Give the position of every Plasmodium parasite visible.
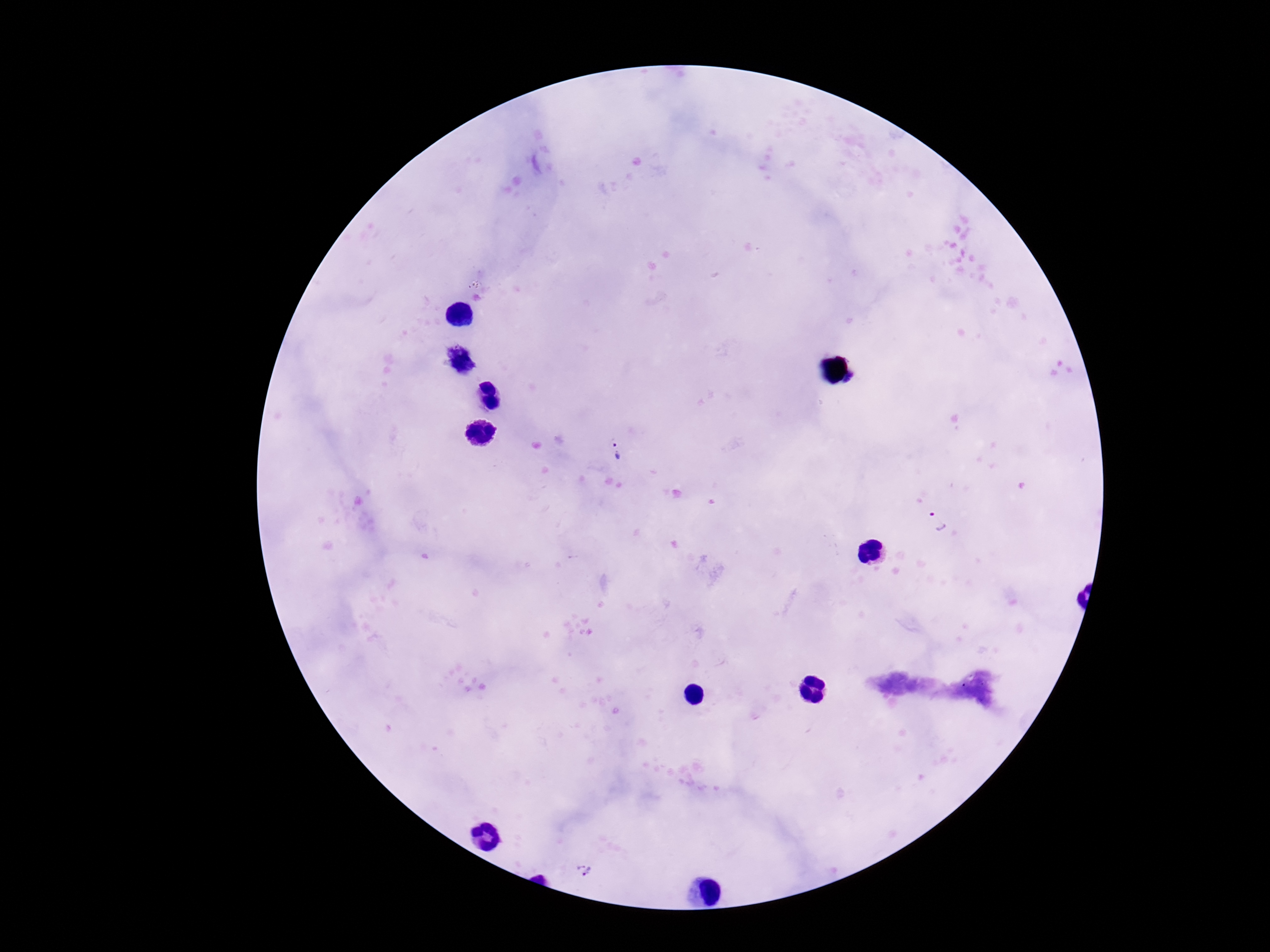
Approximate centers as [x, y] in pixels.
Plasmodium parasites: [614, 454], [937, 522], [585, 870].

stain: Giemsa
patient_malaria_status: infected
capture: smartphone camera through the microscope eyepiece
field_of_view: single
magnification: 100x
preparation: thick blood film
image_size: 1270×952 pixels